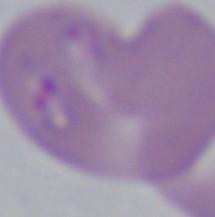 A Babesia parasite is seen. Photomicrograph. 1000x magnification.